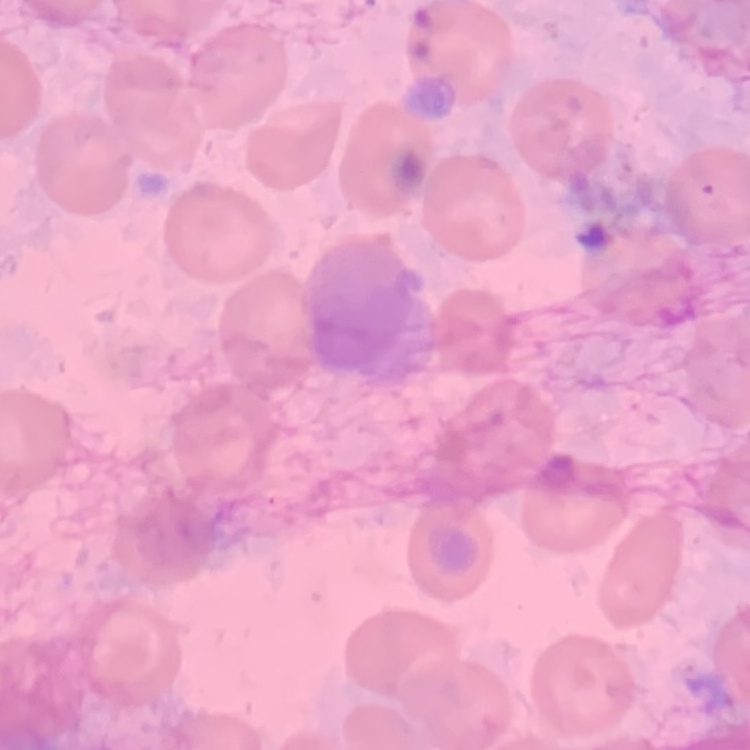
red blood cell morphology = no rouleaux formation
stain = Field's or Giemsa
preparation = thin peripheral smear
image type = one tile cut from a larger photomicrograph